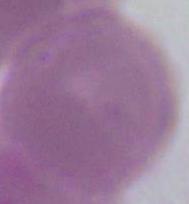
identification = erythrocyte
magnification = 1000x
modality = photomicrograph